Give the position of every malaria parasite.
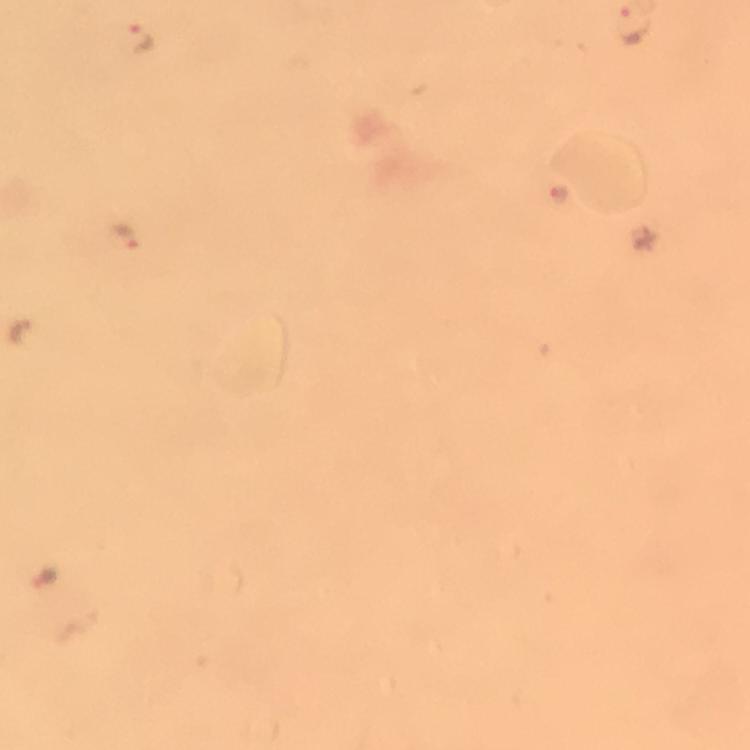

Approximate centers as (x, y) in pixels.
Malaria parasites: (139, 34), (129, 239), (19, 337), (43, 582).

image size = 750×750 pixels
preparation = thick smear
context = from a malaria diagnostic workup
cropped from = a single field of view
magnification = 100x
immersion oil = applied
capture = smartphone photograph through a microscope
stain = Giemsa